Give the position of every Plasmodium parasite.
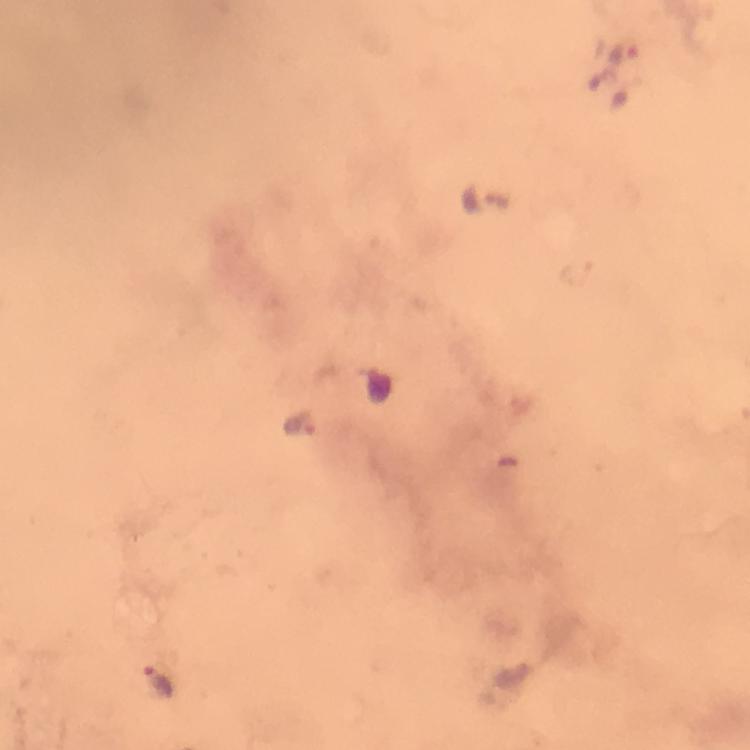

Approximate object centers, in pixels from the top-left corner.
Plasmodium parasites: (x=627, y=56), (x=479, y=198), (x=301, y=425), (x=157, y=677).

Cropped region of a single field of view. Photographed through the microscope with a smartphone camera. Image is 750×750 pixels. At 100x magnification. Immersion oil was used. Thick blood film. Giemsa-stained preparation. From a diagnostic examination for malaria.